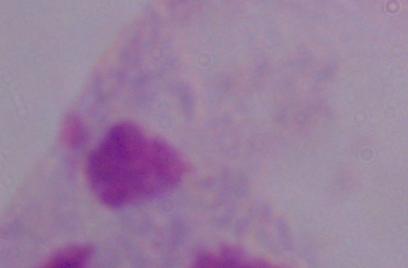
Summary:
  - Identification: trichomonad
  - Magnification: 1000x
  - Modality: micrograph